Name the parasite shown.
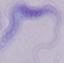

This is a trypanosome.

Captured at 1000x magnification. Micrograph.